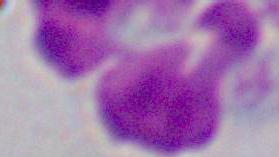

modality: photomicrograph
identification: leukocyte
magnification: 1000x